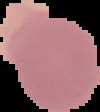 From a thin blood smear. Cell region segmented out of the field of view; the surrounding area is masked to black. Image is 100×112 pixels. Malaria status: uninfected.